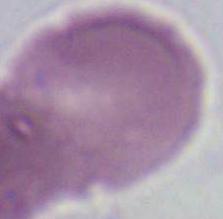

modality: photomicrograph
magnification: 1000x
identification: red blood cell